Describe the morphology of the red blood cells.
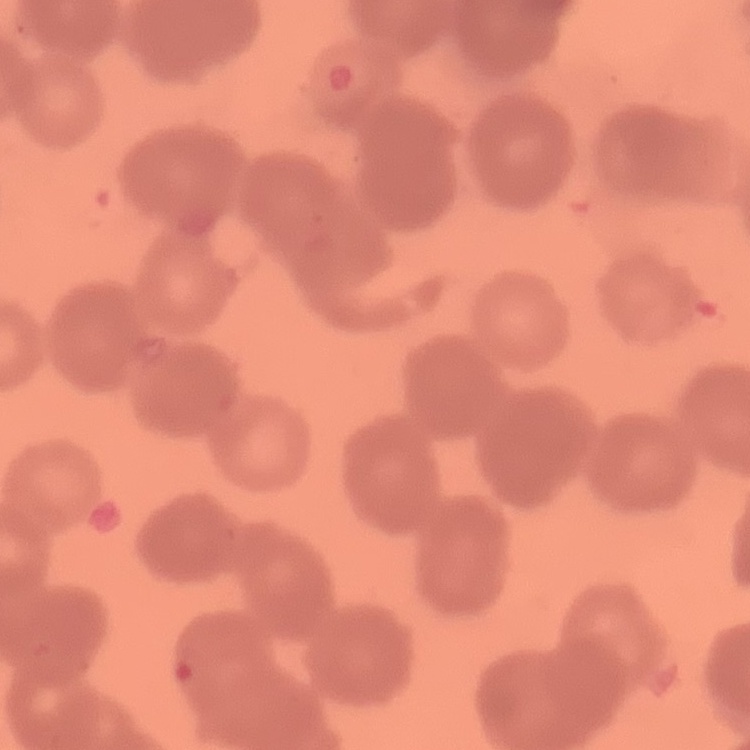
Rouleaux formation.

stain = Field's or Giemsa
preparation = thin blood film
image type = one tile cut from a larger photomicrograph